Report the malaria status of this cell.
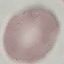
Uninfected.

Summary:
  - Capture: smartphone camera at the microscope eyepiece
  - Stain: Giemsa
  - Preparation: thin smear
  - Image type: automatically extracted cell patch, resized to 64 × 64 pixels